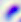

Micrograph. Captured at 400x magnification. Toxoplasma gondii is seen.